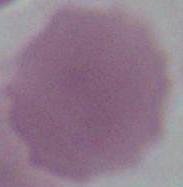 Photomicrograph. An erythrocyte is shown. 1000x magnification.